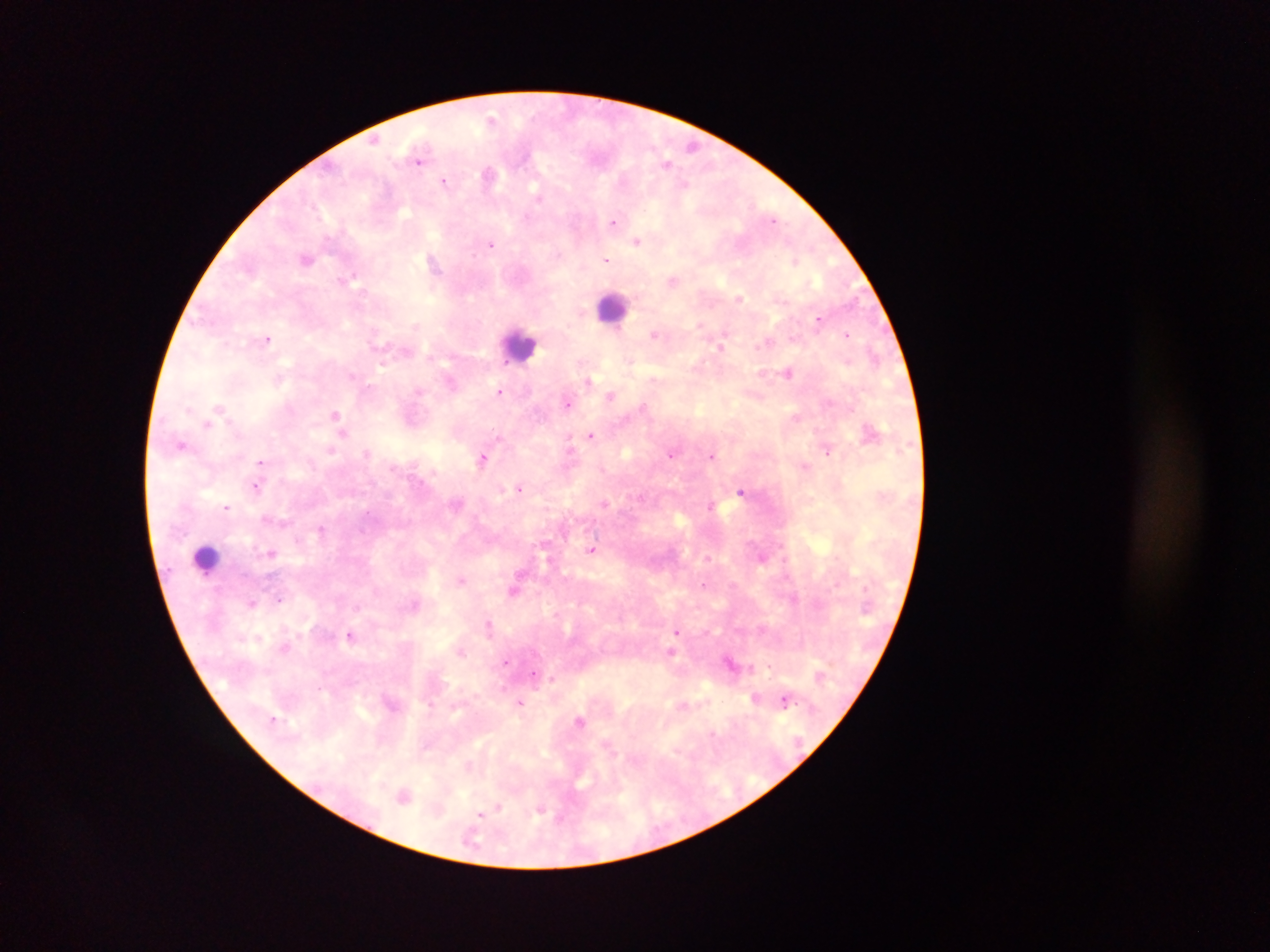

Approximate centers as {x, y} in pixels. Leukocyte locations: {612, 307}, {520, 345}, {206, 558}. Malaria parasite locations: {492, 119}, {374, 140}, {691, 145}, {419, 160}, {666, 163}, {489, 174}, {444, 181}, {539, 196}, {774, 220}, {613, 221}, {637, 241}, {491, 244}, {306, 259}, {433, 261}, {606, 261}, {794, 261}, {353, 277}, {673, 280}, {739, 298}, {818, 320}, {654, 334}, {847, 335}, {268, 339}, {767, 343}, {721, 346}, {504, 362}, {383, 363}, {788, 372}, {654, 378}, {588, 381}, {451, 382}, {418, 391}, {500, 392}, {611, 396}, {567, 402}, {643, 405}, {219, 407}, {189, 409}, {335, 414}, {796, 416}, {207, 425}, {343, 433}, {591, 436}, {569, 443}, {182, 445}, {331, 450}, {828, 452}, {366, 453}, {671, 455}, {712, 455}, {483, 458}, {260, 462}, {804, 466}, {256, 487}, {520, 488}, {740, 492}, {604, 503}, {710, 505}, {226, 507}, {321, 529}, {592, 550}, {271, 553}, {761, 558}, {461, 580}, {704, 584}, {514, 591}, {279, 600}, {252, 603}, {489, 624}, {677, 631}, {350, 635}, {284, 648}, {462, 651}, {670, 651}, {506, 661}, {769, 666}, {534, 673}, {552, 679}, {756, 698}, {785, 700}, {520, 702}, {580, 720}, {404, 796}, {498, 808}, {540, 811}, {481, 814}, {561, 818}. Collected in Ghana. Thick blood smear. One field of view. Mobile-phone photograph taken through the microscope. Image is 1270×952 pixels.